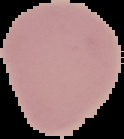

{
  "image_size": "124×139 pixels",
  "preparation": "thin blood smear",
  "image_type": "segmented cell region with the area outside set to black",
  "result": "negative for malaria parasites"
}